Classify this cell by malaria status.
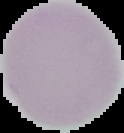

Uninfected.

Image is 124×133 pixels. From a thin blood smear. The area outside the segmented cell region is set to black.